Locate platelets.
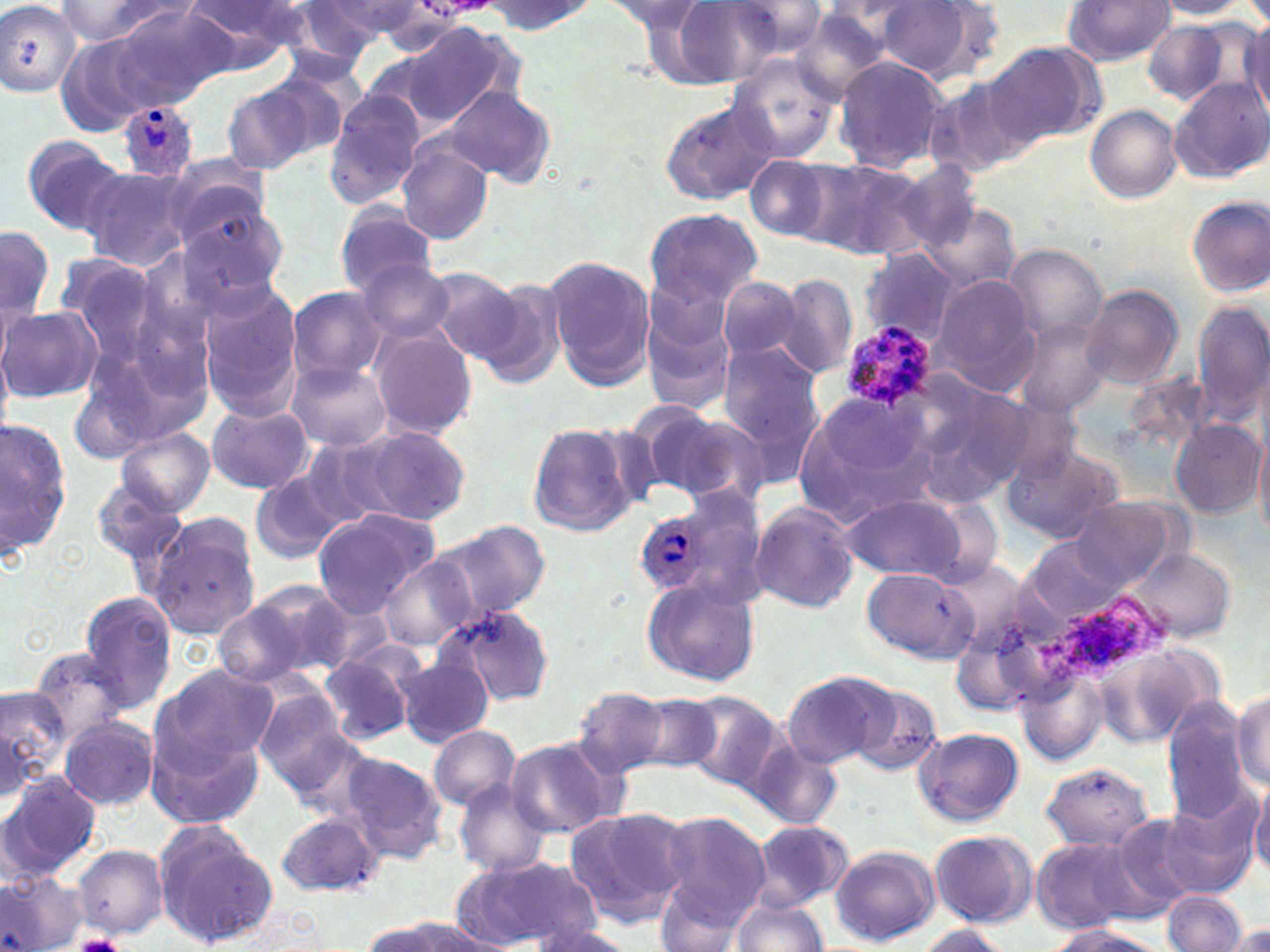
Approximate bounding boxes as [x1, y1, x2, y2] in pixels.
Platelets: [71, 934, 131, 952].

Plasmodium ovale-infected red blood cell locations: [120, 103, 196, 181], [839, 323, 937, 410], [636, 513, 709, 594]. Uninfected red blood cell locations: [0, 0, 82, 98], [602, 0, 708, 34], [660, 0, 782, 87], [1152, 0, 1252, 19], [55, 1, 190, 49], [314, 1, 430, 45], [477, 1, 596, 35], [724, 1, 828, 60], [875, 1, 993, 81], [1062, 1, 1176, 66], [175, 2, 307, 72], [287, 2, 396, 70], [107, 4, 231, 109], [791, 8, 900, 99], [1244, 19, 1270, 120], [1141, 20, 1236, 104], [400, 21, 519, 130], [980, 44, 1100, 149], [727, 53, 842, 164], [833, 55, 952, 174], [927, 79, 1029, 178], [1172, 79, 1270, 185], [221, 81, 322, 176], [443, 83, 556, 187], [323, 91, 422, 208], [659, 96, 780, 205], [1085, 105, 1182, 203], [21, 134, 129, 236], [394, 143, 495, 245], [744, 155, 833, 242], [809, 156, 930, 259], [891, 156, 986, 254], [161, 158, 276, 253], [79, 166, 193, 271], [1185, 195, 1270, 297], [923, 203, 1021, 295], [333, 204, 437, 296], [644, 208, 764, 308], [173, 212, 289, 309], [1, 224, 55, 324], [1006, 244, 1107, 340], [858, 250, 959, 346], [51, 252, 166, 372], [545, 255, 655, 390], [356, 257, 457, 344], [423, 267, 526, 358], [775, 274, 857, 380], [931, 274, 1042, 394], [716, 277, 805, 362], [472, 278, 570, 387], [199, 283, 305, 420], [1080, 284, 1184, 390], [287, 286, 387, 384], [641, 301, 739, 414], [1192, 302, 1267, 422], [1, 304, 102, 404], [1012, 318, 1114, 417], [369, 328, 477, 439], [718, 342, 825, 445], [286, 361, 392, 451], [909, 377, 1031, 499], [810, 391, 927, 489], [204, 403, 314, 494], [644, 406, 769, 508], [0, 415, 75, 565], [526, 420, 638, 536], [1172, 420, 1264, 516], [115, 426, 215, 515], [358, 426, 472, 524], [1254, 427, 1270, 543], [297, 434, 415, 529], [1002, 444, 1125, 545], [248, 473, 344, 567], [91, 476, 187, 568], [841, 495, 970, 582], [1071, 497, 1182, 589], [748, 502, 860, 613], [311, 510, 438, 615], [148, 516, 262, 641], [435, 520, 550, 619], [1025, 535, 1126, 623], [1124, 545, 1237, 644], [378, 555, 480, 652], [863, 567, 977, 663], [643, 577, 761, 687], [242, 578, 356, 676], [79, 591, 180, 713], [212, 598, 325, 691], [439, 605, 557, 705], [29, 647, 132, 746], [319, 647, 422, 745], [396, 657, 492, 748], [150, 663, 278, 775], [782, 671, 894, 769], [1016, 671, 1103, 765], [849, 682, 944, 776], [0, 683, 69, 791], [571, 687, 673, 777], [1233, 687, 1270, 792], [253, 692, 357, 797], [685, 692, 787, 791], [1200, 692, 1269, 808], [633, 695, 721, 774], [1163, 702, 1250, 826], [60, 716, 158, 810], [144, 723, 265, 833], [428, 725, 523, 812], [914, 725, 1024, 826], [503, 737, 621, 839], [748, 739, 842, 831], [336, 751, 447, 865], [1040, 761, 1156, 851], [1, 771, 103, 882], [454, 780, 553, 876], [1250, 782, 1270, 875], [1139, 803, 1256, 902], [563, 807, 691, 929], [655, 811, 770, 925], [277, 812, 381, 893], [1113, 813, 1211, 907], [746, 820, 854, 912], [152, 822, 280, 950], [928, 829, 1037, 930], [1030, 836, 1154, 934], [72, 843, 168, 938], [830, 845, 940, 946], [455, 851, 602, 946], [0, 869, 86, 952], [655, 880, 754, 952], [1161, 890, 1249, 952], [729, 899, 830, 952], [360, 919, 462, 952], [521, 923, 636, 952], [1224, 923, 1270, 951], [911, 924, 1012, 951], [1046, 925, 1171, 952]. Slide-level diagnosis: Plasmodium ovale. Thin blood film. Optical microscopy. Captured at 1000x magnification. May-Grünwald-Giemsa-stained preparation. One field of a larger specimen. Image is 1270×952 pixels.